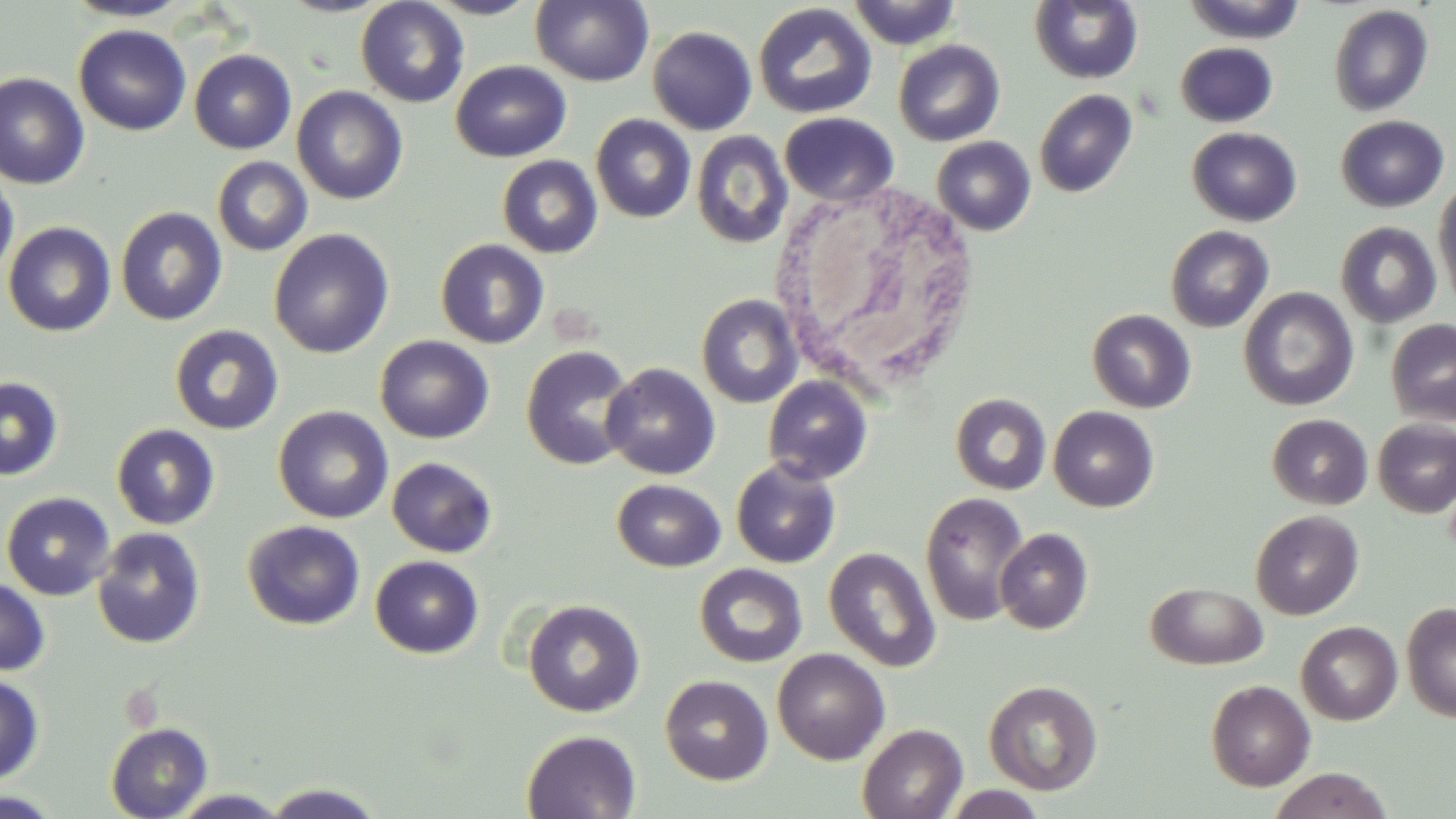

Summary:
  - Coordinate format: approximate bounding boxes as (x1, y1, x2, y2) in pixels
  - Uninfected red blood cell locations: (62, 0, 194, 22), (276, 0, 394, 17), (424, 0, 542, 19), (847, 0, 963, 49), (1182, 0, 1309, 44), (355, 1, 470, 108), (531, 1, 654, 87), (1029, 1, 1143, 84), (752, 3, 878, 120), (1328, 4, 1434, 116), (73, 24, 192, 136), (647, 26, 758, 135), (893, 39, 1005, 146), (1179, 39, 1284, 219), (1175, 42, 1278, 127), (189, 49, 297, 154), (450, 60, 571, 162), (0, 72, 91, 189), (292, 86, 408, 205), (1034, 89, 1137, 198), (779, 111, 899, 207), (591, 114, 696, 223), (1336, 115, 1450, 212), (1187, 126, 1302, 227), (691, 130, 793, 249), (932, 136, 1036, 235), (497, 154, 603, 258), (212, 156, 313, 257), (0, 169, 19, 286), (1433, 178, 1456, 313), (115, 206, 227, 326), (3, 221, 116, 337), (1335, 221, 1442, 328), (1165, 225, 1274, 332), (268, 228, 394, 359), (435, 238, 550, 349), (1239, 287, 1358, 411), (696, 294, 803, 408), (1087, 309, 1196, 413), (1386, 318, 1456, 426), (169, 324, 284, 435), (375, 335, 494, 443), (520, 345, 638, 470), (601, 363, 720, 480), (763, 375, 873, 485), (0, 376, 64, 481), (950, 392, 1052, 495), (273, 406, 393, 523), (1048, 406, 1159, 512), (1267, 414, 1373, 510), (1372, 418, 1456, 518), (111, 424, 220, 530), (386, 456, 497, 557), (731, 458, 841, 568), (612, 479, 726, 572), (1, 491, 116, 600), (919, 492, 1030, 626), (1250, 510, 1364, 620), (242, 520, 365, 630), (92, 527, 206, 649), (995, 528, 1093, 634), (824, 547, 941, 672), (370, 555, 484, 658), (695, 564, 807, 668), (0, 576, 50, 676), (1146, 582, 1268, 670), (523, 599, 645, 717), (1401, 601, 1456, 722), (1296, 621, 1402, 725), (773, 648, 890, 765), (0, 672, 45, 784), (660, 675, 773, 786), (984, 679, 1103, 796), (1206, 679, 1315, 791), (106, 722, 212, 819), (857, 723, 968, 819), (522, 729, 641, 818), (1267, 768, 1395, 819), (259, 782, 390, 818), (938, 785, 1049, 819), (167, 789, 294, 818)
  - White blood cell locations: (771, 179, 979, 403)
  - Slide-level diagnosis: negative for blood parasites
  - Field of view: one of a larger specimen
  - Modality: light microscopy
  - Stain: May-Grünwald-Giemsa
  - Magnification: 1000x
  - Image size: 1456×819 pixels
  - Preparation: thin blood film